Give the preparation type.
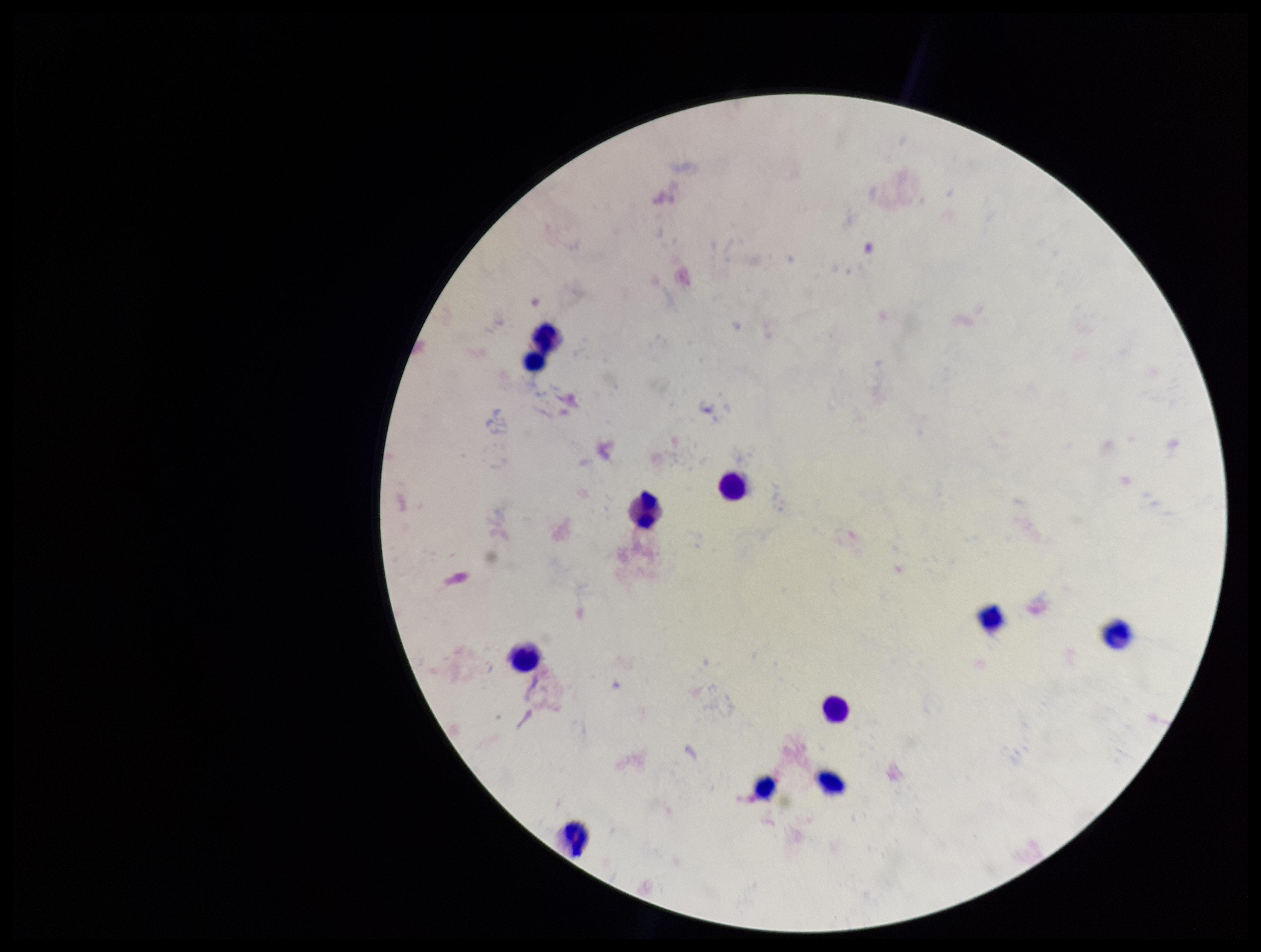
Thick.

Summary:
  - Field of view: one from this slide
  - Image size: 1261×952 pixels
  - Stain: Giemsa
  - Capture: smartphone photograph through the microscope eyepiece
  - Patient malaria status: negative
  - Parasite count: 0
  - Plasmodium parasites: none seen
  - Leukocyte count: 11